Locate every Plasmodium parasite and every leukocyte.
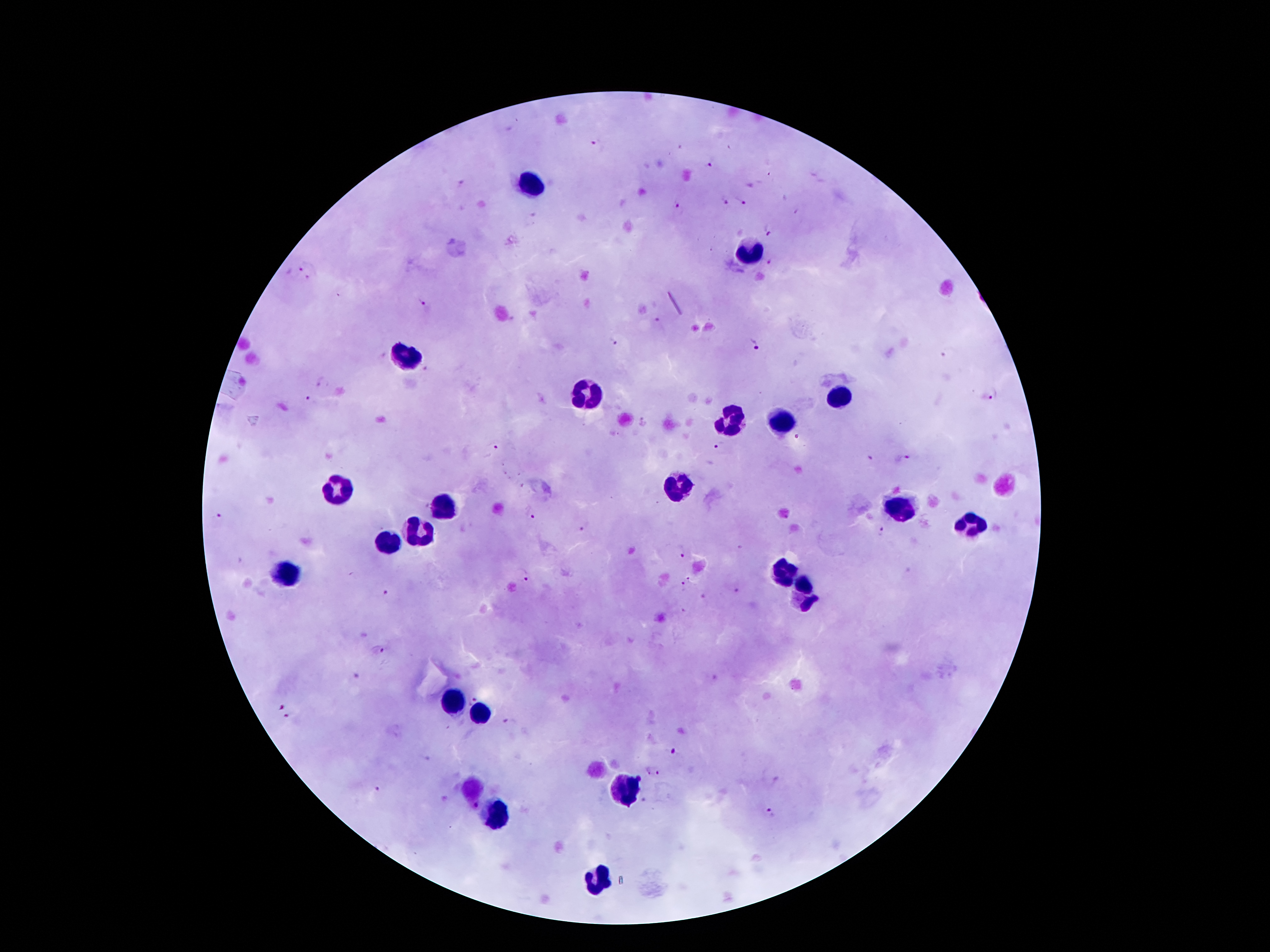
Approximate centers as [x, y] in pixels.
Plasmodium parasites: [596, 143], [709, 163], [462, 183], [725, 200], [742, 200], [677, 204], [771, 230], [304, 266], [311, 279], [423, 302], [658, 323], [615, 339], [753, 343], [321, 384], [994, 395], [310, 400], [719, 446], [498, 448], [871, 459], [903, 460], [529, 515], [218, 519], [585, 528], [882, 534], [678, 553], [523, 576], [690, 579], [682, 588], [735, 592], [385, 593], [685, 610], [379, 650], [475, 697], [278, 706], [288, 717], [508, 722], [674, 752], [425, 758], [652, 772], [378, 787], [474, 806], [771, 814].
Leukocytes: [532, 184], [749, 251], [407, 358], [589, 395], [835, 395], [730, 419], [782, 423], [337, 486], [677, 487], [446, 505], [902, 507], [970, 524], [425, 530], [383, 541], [284, 572], [779, 572], [806, 595], [452, 703], [482, 713], [470, 789], [626, 793], [493, 816], [599, 880].

image size = 1270×952 pixels
patient malaria status = infected with Plasmodium falciparum
magnification = 100x
preparation = thick blood smear
field of view = one from this slide
stain = Giemsa
capture = smartphone camera through the microscope eyepiece